Assess this cell for malaria.
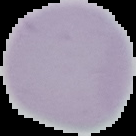
It is uninfected.

image type = segmented cell region with the area outside set to black
preparation = thin blood film
image size = 136×136 pixels